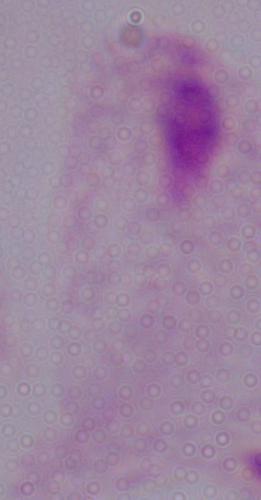
modality = micrograph
identification = trichomonad
magnification = 1000x